Give the preparation type.
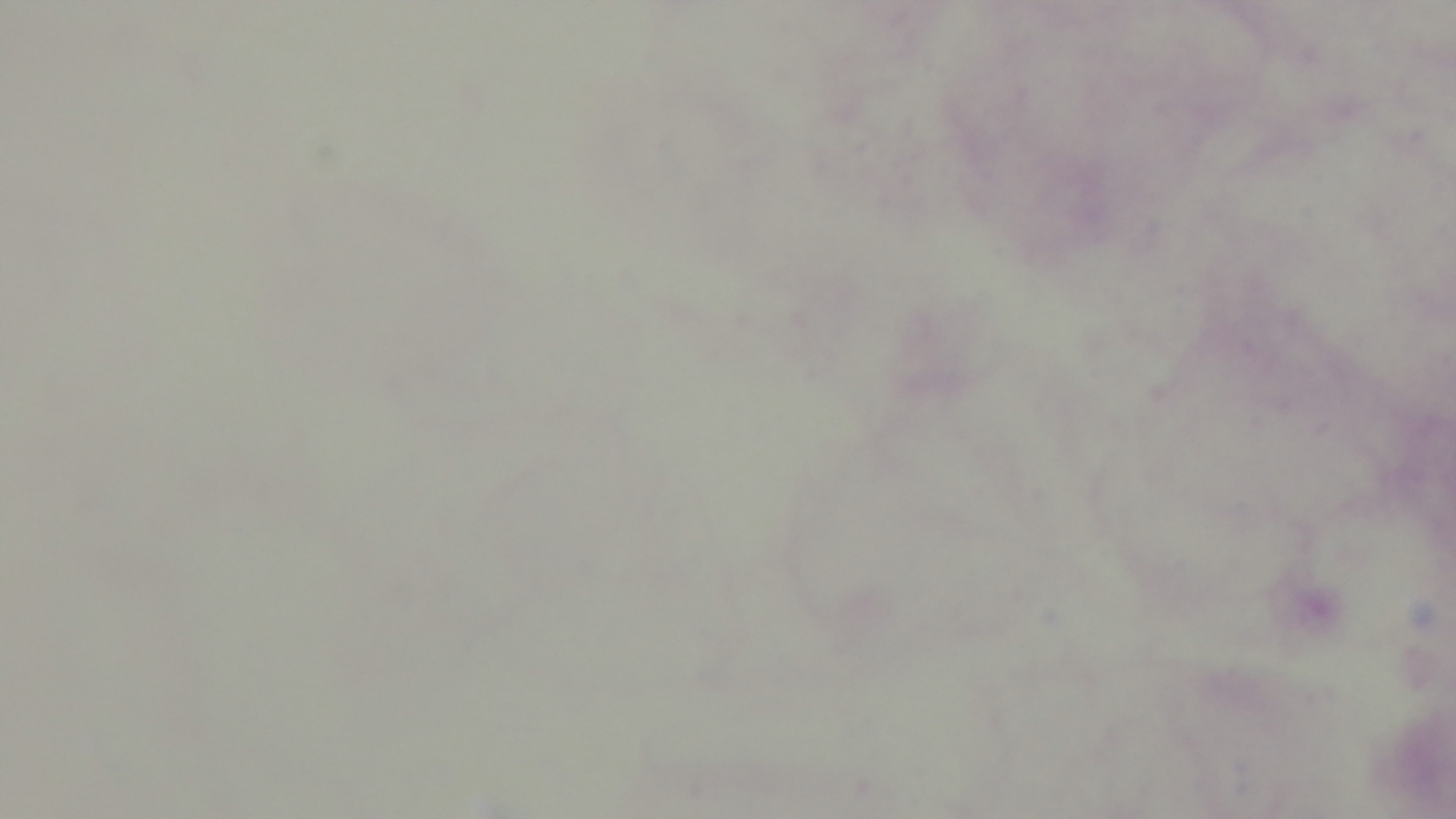

It is a thick blood film.

Malaria status: uninfected. One field from the slide. Giemsa-stained. Oil-immersion objective, 100x. Captured with a mounted 4K digital camera. Photomicrograph.